Give the position of every Plasmodium parasite visible.
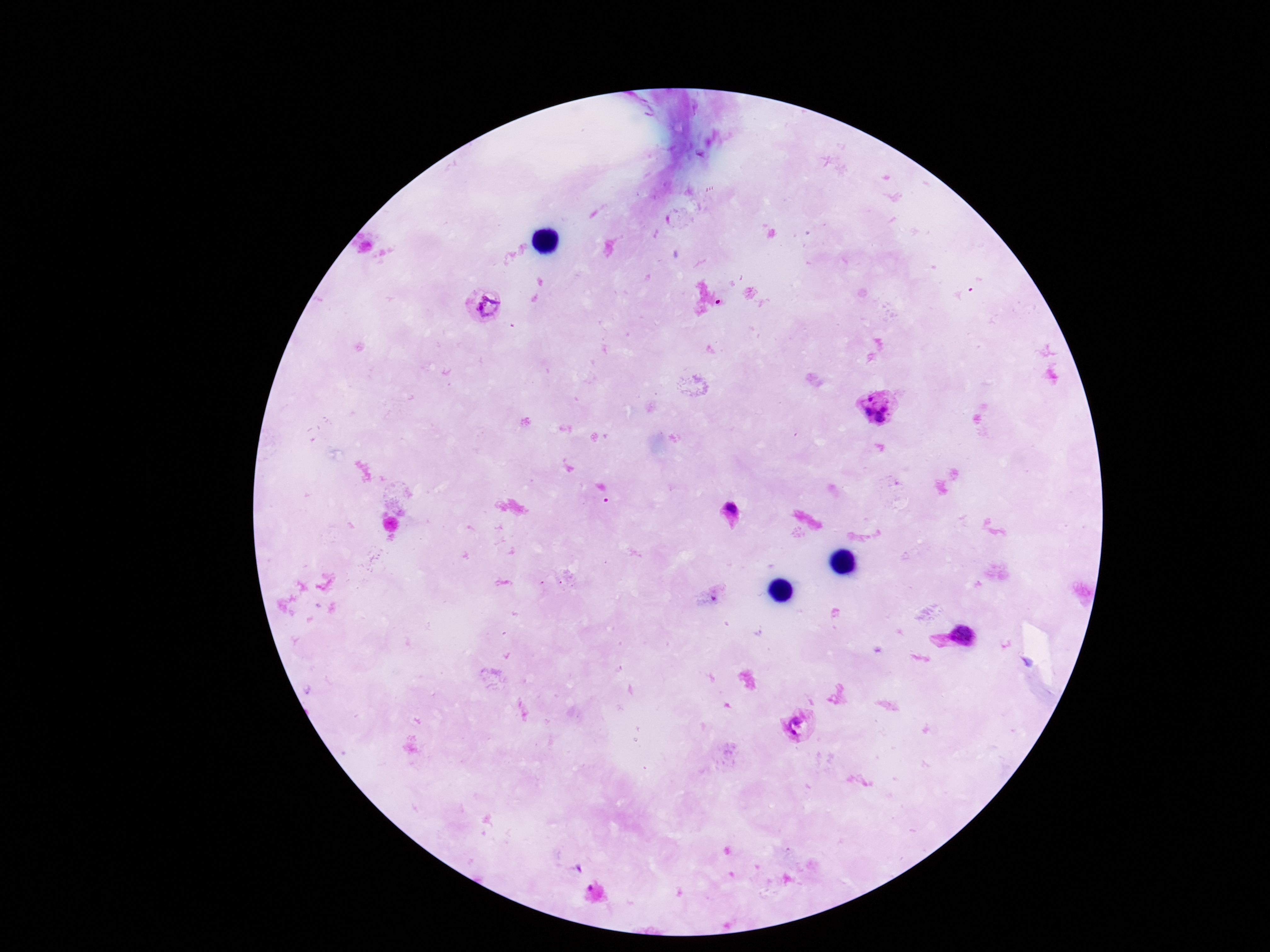
Approximate centers as {x, y} in pixels.
Plasmodium parasites: {489, 307}, {880, 411}, {734, 515}, {961, 636}, {797, 726}.

Summary:
  - Patient malaria status: infected
  - Field of view: single
  - Image size: 1270×952 pixels
  - Capture: smartphone camera through the microscope eyepiece
  - Magnification: 100x
  - Preparation: thick blood film
  - Stain: Giemsa